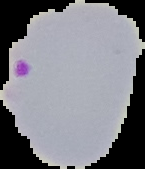
{
  "image_type": "segmented cell region with the area outside set to black",
  "preparation": "thin blood film",
  "image_size": "145×169 pixels",
  "malaria_status": "parasitized"
}